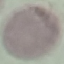

Summary:
  - Malaria status: uninfected
  - Capture: smartphone through the microscope eyepiece
  - Stain: Giemsa
  - Preparation: thin blood smear
  - Image type: cell patch, automatically extracted from a larger field of view and resized to 64 × 64 pixels